Classify this cell by malaria status.
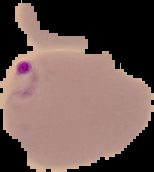

Parasitized.

Summary:
  - Image size: 154×172 pixels
  - Preparation: thin blood smear
  - Image type: segmented cell region on a black background